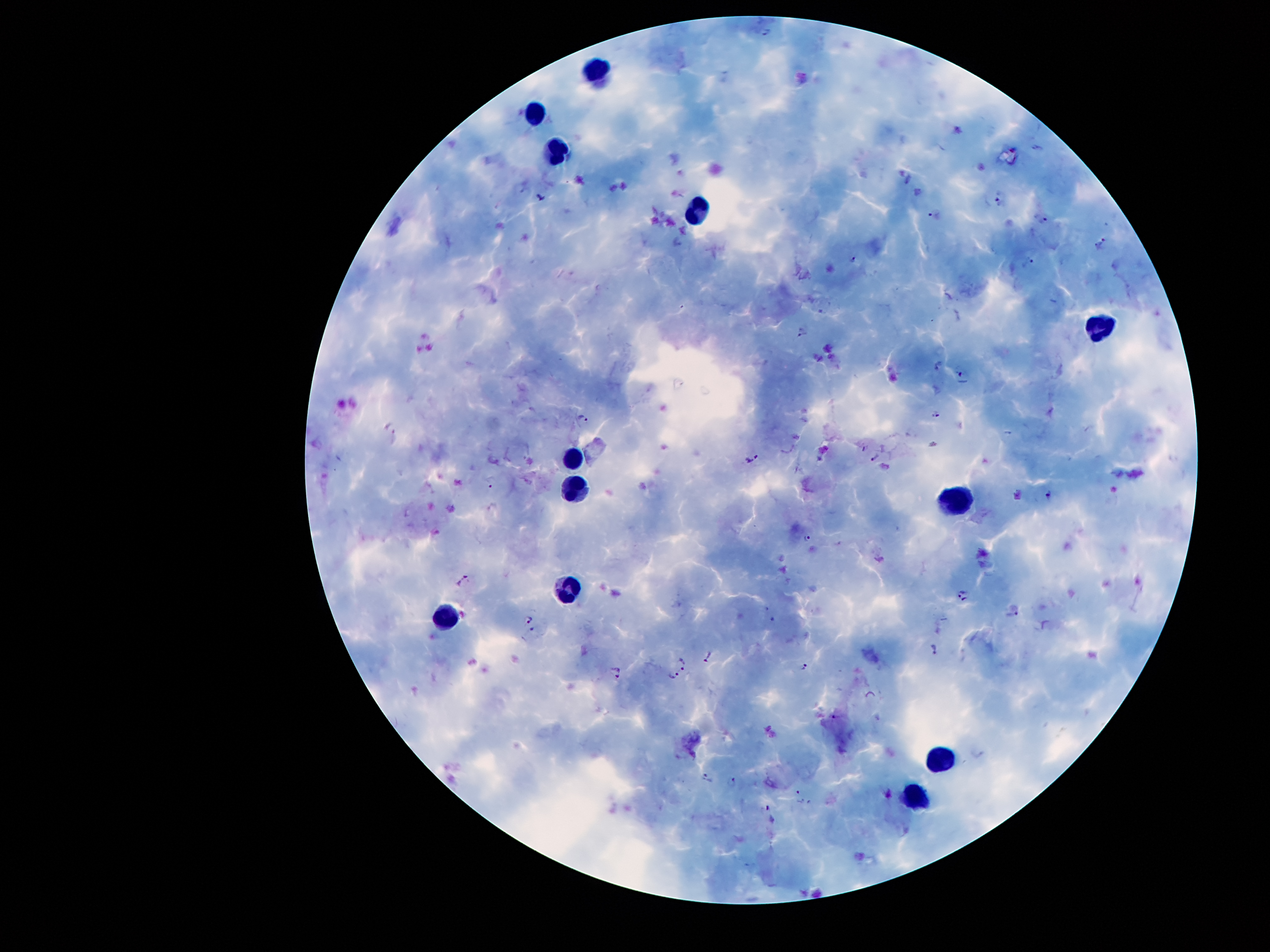

coordinate format = approximate centers as (x, y) in pixels
leukocyte locations = (592, 69), (534, 110), (556, 153), (695, 213), (1098, 325), (573, 457), (577, 490), (956, 500), (568, 588), (444, 619), (938, 758), (917, 794)
malaria parasite locations = (766, 33), (540, 197), (1000, 199), (933, 215), (1041, 219), (1103, 242), (854, 260), (1028, 263), (802, 334), (937, 366), (962, 376), (938, 416), (584, 420), (391, 428), (876, 458), (753, 460), (492, 481), (1050, 495), (807, 539), (465, 579), (964, 595), (1013, 615), (530, 620), (533, 629), (934, 649), (710, 657), (685, 663), (805, 666), (618, 670), (670, 678), (835, 719), (706, 776), (732, 782), (800, 796), (771, 814)
field of view = one from this slide
stain = Giemsa
patient malaria status = positive for Plasmodium falciparum
image size = 1270×952 pixels
capture = smartphone camera through the microscope eyepiece
magnification = 100x
preparation = thick blood film